Evaluate for Plasmodium parasites.
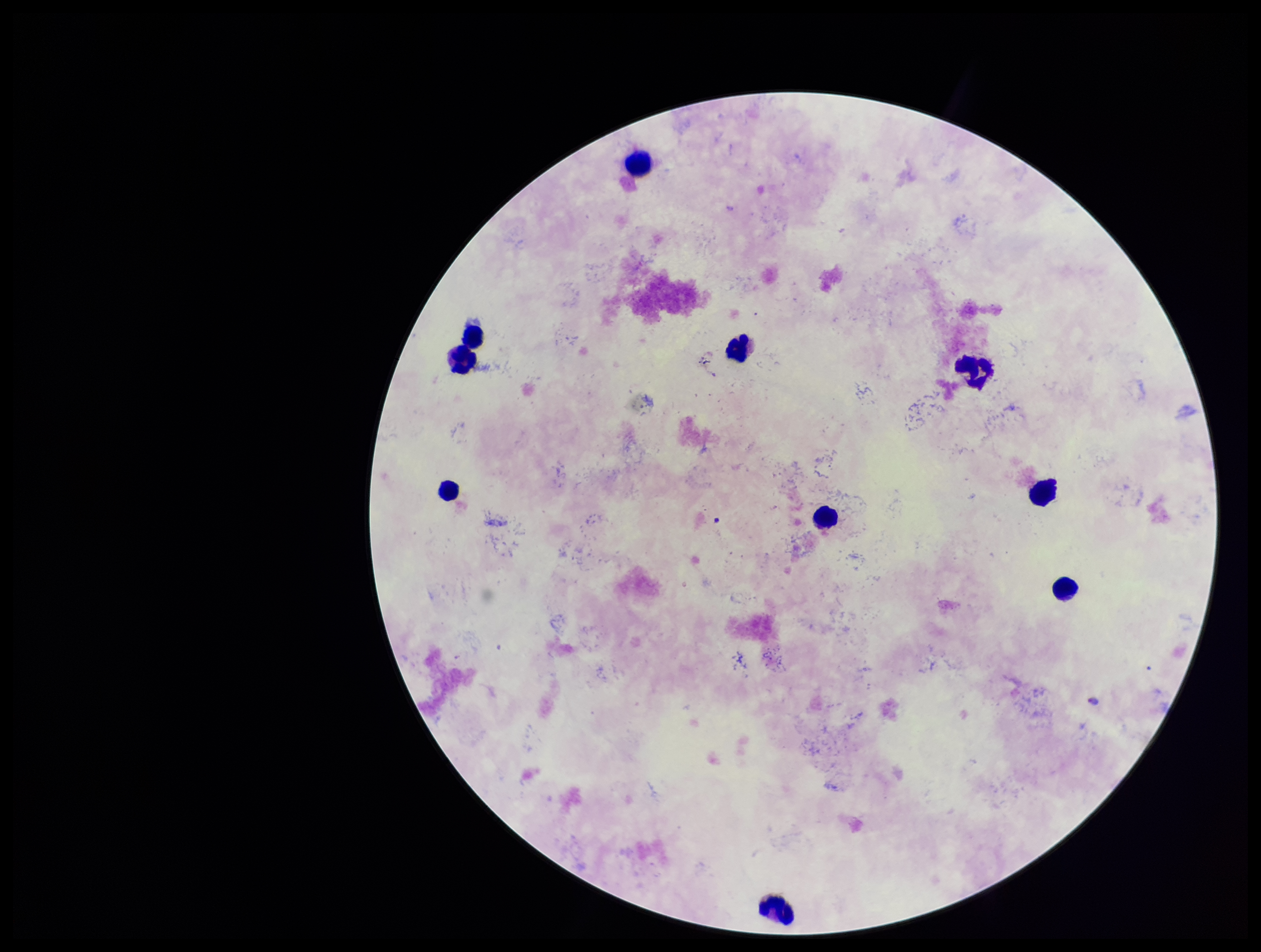
Identified.

parasite count = 1
field of view = single
patient malaria status = positive
preparation = thick smear
capture = smartphone photograph through the microscope eyepiece
species reported for this patient = Plasmodium falciparum
image size = 1261×952 pixels
stain = Giemsa
leukocyte count = 10